Give the position of every Plasmodium parasite visible.
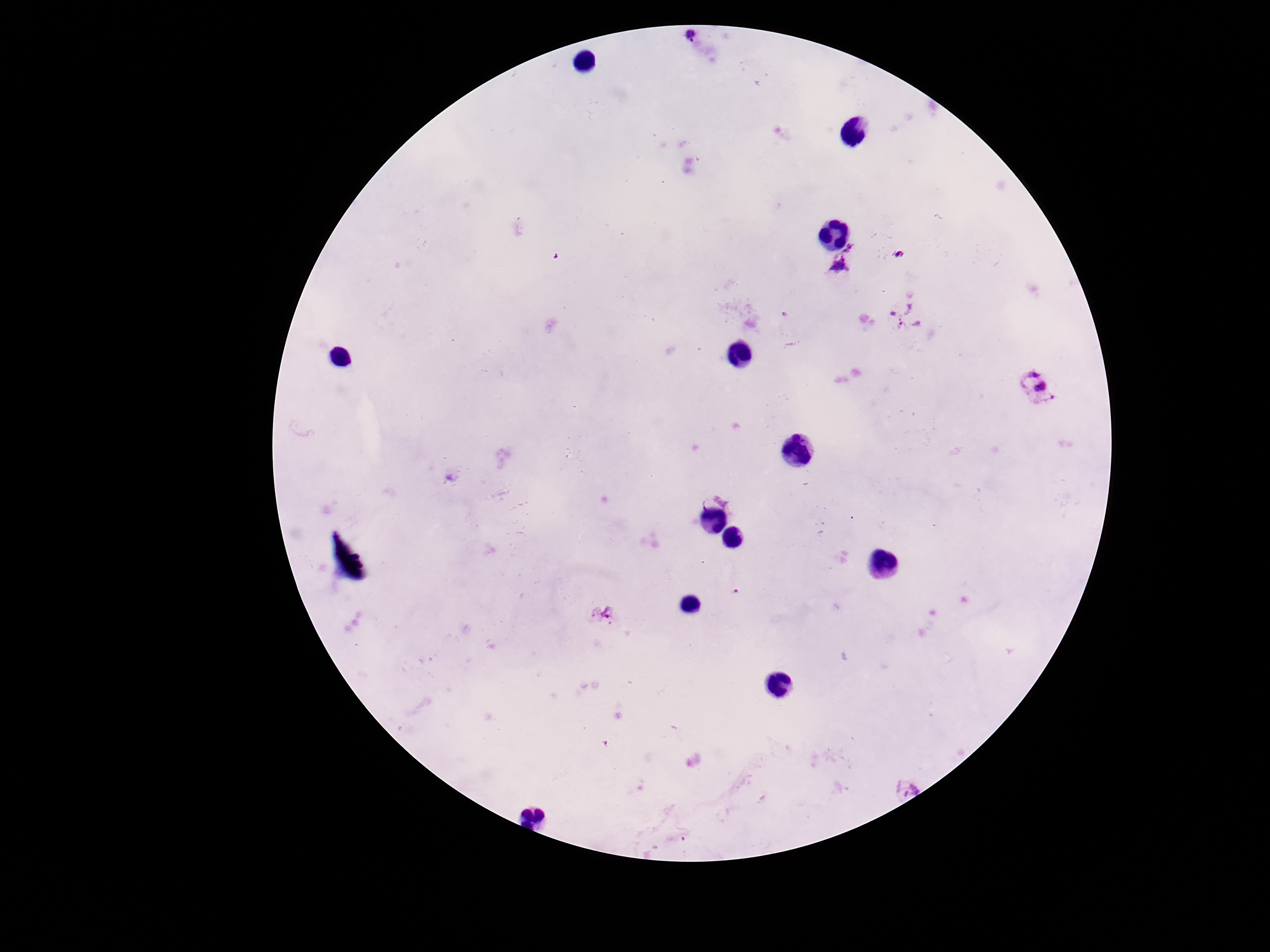
Approximate centers as (x, y) in pixels.
Plasmodium parasites: (694, 47), (847, 266), (906, 318), (1038, 388), (715, 495), (604, 614), (902, 779).

Summary:
  - Capture: smartphone camera through the microscope eyepiece
  - Patient malaria status: infected
  - Field of view: single
  - Magnification: 100x
  - Stain: Giemsa
  - Image size: 1270×952 pixels
  - Preparation: thick peripheral-blood smear